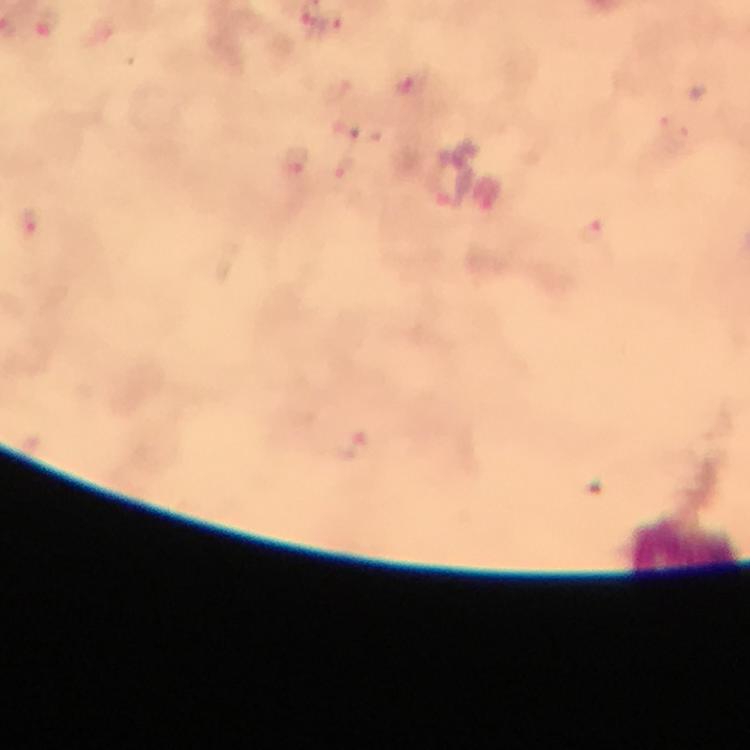

Approximate centers as [x, y] in pixels.
Summary:
  - Leukocyte locations: [682, 542]
  - Malaria parasite locations: [410, 84], [297, 163], [345, 170], [28, 224], [592, 229]
  - Preparation: thick blood smear
  - Immersion oil: applied
  - Image size: 750×750 pixels
  - Magnification: 100x
  - Capture: smartphone camera through the microscope
  - Context: from a malaria diagnostic workup
  - Cropped from: one field of view
  - Stain: Giemsa